Assess this cell for malaria.
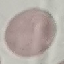

Uninfected.

{
  "stain": "Giemsa",
  "preparation": "thin blood film",
  "image_type": "cell patch, automatically extracted from a larger field of view and resized to 64 × 64 pixels",
  "capture": "smartphone camera at the microscope eyepiece"
}